Report the malaria status of this cell.
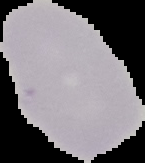

Uninfected.

Summary:
  - Preparation: thin blood film
  - Image type: segmented cell region with the area outside set to black
  - Image size: 145×163 pixels